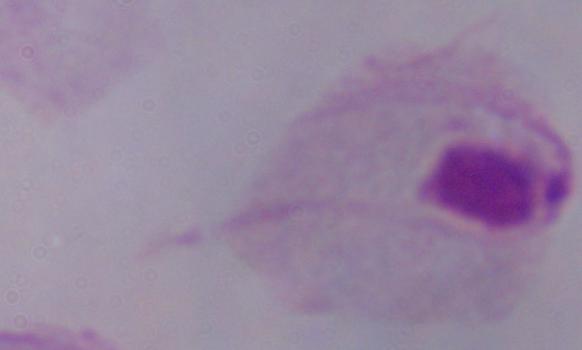

identification = trichomonad
modality = micrograph
magnification = 1000x